Name the parasite shown.
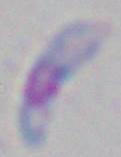
This is Toxoplasma gondii.

1000x magnification. Micrograph.